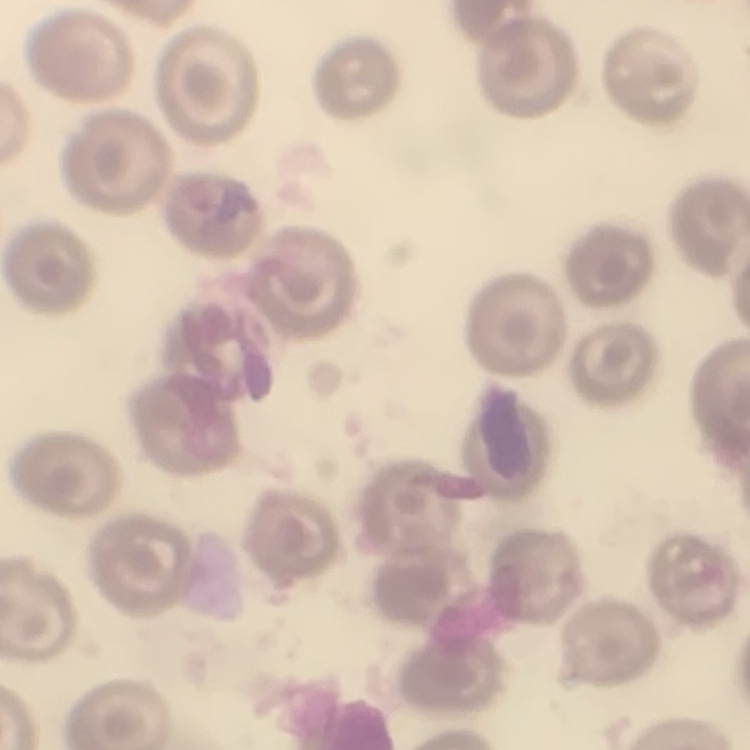 The red blood cells exhibit no rouleaux formation. Square crop of a larger photomicrograph. Thin blood film. Stained with either Field's or Giemsa.